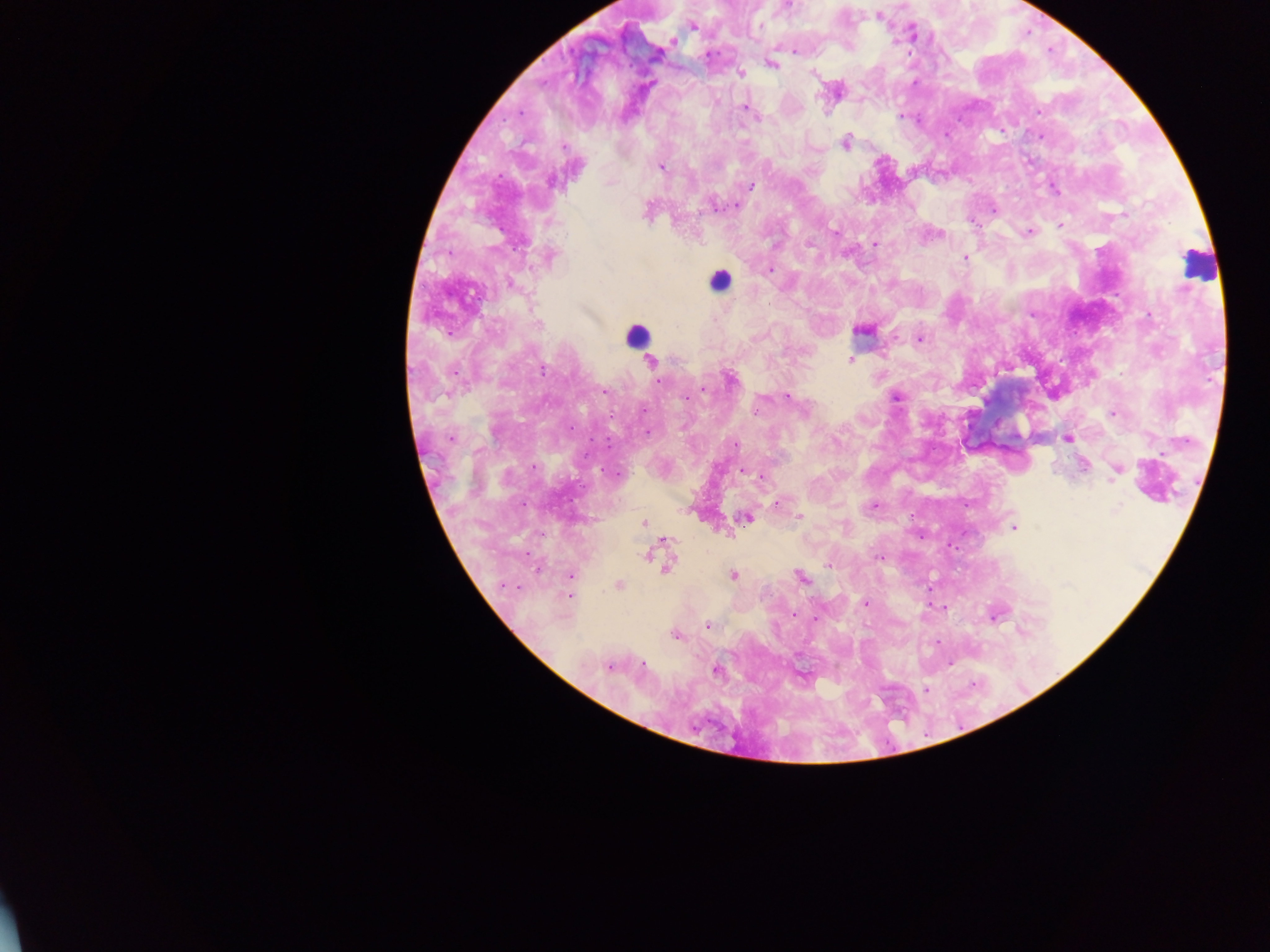
{
  "preparation": "thick blood smear",
  "capture": "mobile-phone photograph through a microscope",
  "field_of_view": "single",
  "country": "Ghana",
  "malaria_parasite_locations": "approximate centers as [x, y] in pixels: [789, 5], [878, 16], [761, 25], [692, 26], [672, 41], [794, 51], [772, 64], [740, 74], [813, 74], [744, 108], [1039, 111], [901, 116], [845, 142], [661, 167], [752, 185], [1054, 189], [737, 206], [716, 207], [995, 209], [648, 210], [1124, 214], [1060, 225], [835, 232], [1029, 232], [940, 234], [875, 244], [774, 245], [551, 256], [965, 258], [770, 270], [512, 284], [1150, 316], [539, 325], [862, 330], [920, 339], [850, 359], [652, 361], [541, 371], [731, 380], [658, 381], [702, 389], [604, 391], [787, 396], [897, 397], [756, 410], [1113, 413], [648, 431], [450, 438], [1068, 439], [735, 445], [1083, 466], [743, 471], [1117, 471], [759, 476], [776, 503], [874, 505], [1118, 509], [800, 516], [745, 518], [644, 522], [1014, 527], [668, 541], [647, 555], [878, 557], [829, 565], [666, 566], [570, 575], [733, 575], [801, 577], [504, 585], [619, 585], [570, 597], [865, 603], [794, 614], [996, 615], [708, 626], [675, 635], [609, 667], [716, 670], [925, 690]",
  "image_size": "1270×952 pixels",
  "leukocyte_locations": "approximate centers as [x, y] in pixels: [1195, 265], [719, 281], [637, 336]"
}